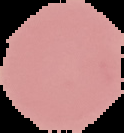

Cell region segmented out of the field of view; the surrounding area is masked to black. From a thin blood film. Result: no malaria parasites seen. Image is 124×133 pixels.